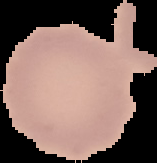 Result: no Plasmodium parasites detected. The area outside the segmented cell region is set to black. From a thin blood film. Image is 157×163 pixels.